Describe the morphology of the red blood cells.
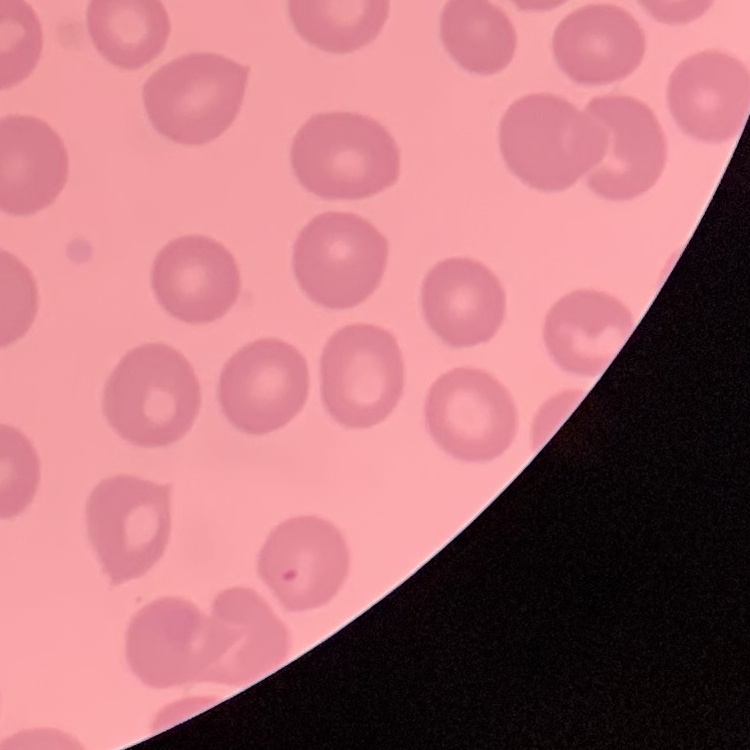
No rouleaux formation.

Summary:
  - Stain: Field's or Giemsa
  - Preparation: thin blood smear
  - Image type: one tile cut from a larger photomicrograph